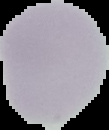
image_size: 109×130 pixels
image_type: segmented cell region on a black background
malaria_status: uninfected
preparation: thin blood smear